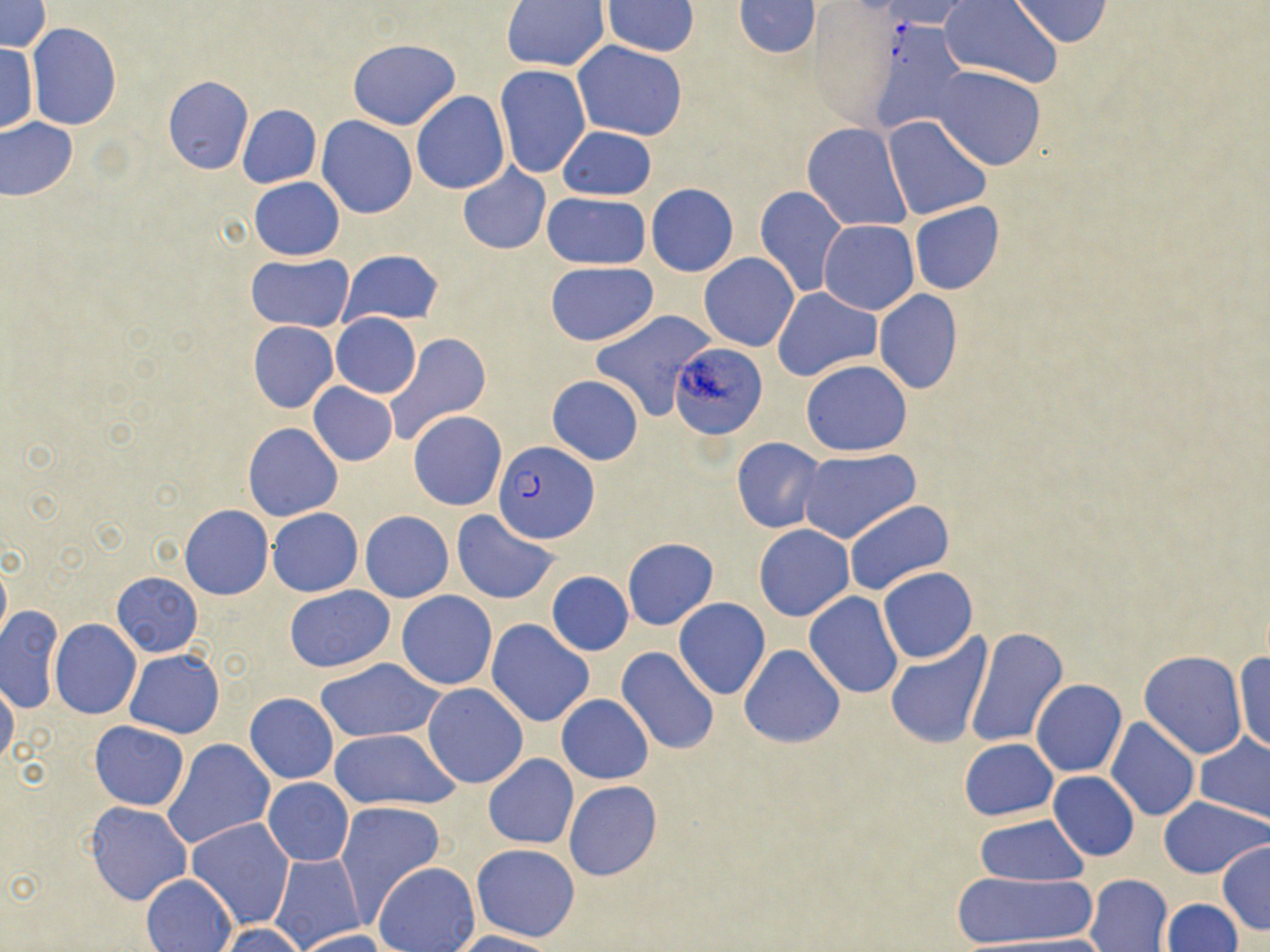

{
  "slide_level_diagnosis": "Plasmodium falciparum",
  "magnification": "1000x",
  "uninfected_red_blood_cell_locations": "approximate bounding boxes as (x1,y1)-(x2,y2) corner pairs in pixels: (1008,0)-(1113,48), (0,1)-(51,53), (601,1)-(700,57), (733,1)-(820,58), (503,2)-(611,72), (886,2)-(974,31), (940,2)-(1062,86), (806,7)-(894,126), (27,24)-(122,129), (346,38)-(459,131), (572,39)-(688,140), (1,43)-(38,133), (495,64)-(590,178), (934,67)-(1045,170), (163,76)-(253,174), (412,91)-(509,194), (237,104)-(320,188), (318,107)-(507,206), (317,116)-(418,218), (884,117)-(990,218), (0,118)-(77,200), (802,123)-(911,231), (558,125)-(657,200), (458,165)-(550,255), (248,177)-(344,260), (646,183)-(739,276), (755,186)-(847,298), (541,191)-(651,269), (909,201)-(1004,295), (818,220)-(919,314), (339,249)-(445,328), (248,253)-(353,332), (699,253)-(799,351), (546,262)-(657,345), (773,288)-(881,381), (873,290)-(963,395), (590,310)-(715,420), (331,313)-(422,397), (248,321)-(340,413), (385,333)-(491,442), (670,344)-(766,440), (801,360)-(911,456), (546,374)-(644,466), (309,382)-(397,465), (262,390)-(387,492), (409,411)-(507,511), (244,423)-(342,521), (733,437)-(827,533), (798,448)-(919,544), (844,500)-(953,597), (180,505)-(273,599), (267,507)-(362,597), (361,511)-(453,602), (451,511)-(561,605), (755,524)-(853,621), (622,538)-(718,629), (0,556)-(11,647), (877,567)-(978,663), (111,572)-(203,655), (547,572)-(633,655), (284,585)-(394,673), (397,591)-(497,689), (805,592)-(903,698), (673,598)-(771,699), (1,605)-(63,713), (486,619)-(595,726), (50,620)-(141,719), (964,626)-(1068,749), (885,635)-(992,751), (739,643)-(845,748), (615,647)-(719,755), (124,649)-(224,739), (1139,650)-(1249,758), (1233,652)-(1269,756), (314,658)-(445,743), (0,679)-(19,769), (1030,679)-(1126,777), (421,683)-(528,788), (245,693)-(339,783), (556,694)-(653,784), (1105,717)-(1198,821), (91,721)-(188,810), (329,729)-(459,810), (1194,734)-(1270,823), (163,738)-(276,848), (960,738)-(1057,820), (484,754)-(578,849), (1048,772)-(1139,861), (119,778)-(262,891), (263,779)-(354,866), (565,781)-(661,881), (1158,797)-(1270,877), (335,800)-(445,918), (86,802)-(191,905), (975,815)-(1088,886), (188,818)-(295,929), (1216,841)-(1270,935), (471,843)-(579,942), (267,851)-(366,950), (374,862)-(479,952), (947,871)-(1101,948), (140,873)-(236,952), (1084,874)-(1173,952), (1161,898)-(1242,951), (215,923)-(312,952), (291,928)-(392,952), (449,930)-(559,952)",
  "preparation": "thin blood smear",
  "modality": "optical microscopy",
  "stain": "May-Grünwald-Giemsa",
  "image_size": "1270×952 pixels",
  "field_of_view": "single",
  "plasmodium_falciparum_infected_red_blood_cell_locations": "approximate bounding boxes as (x1,y1)-(x2,y2) corner pairs in pixels: (493,441)-(599,543)"
}